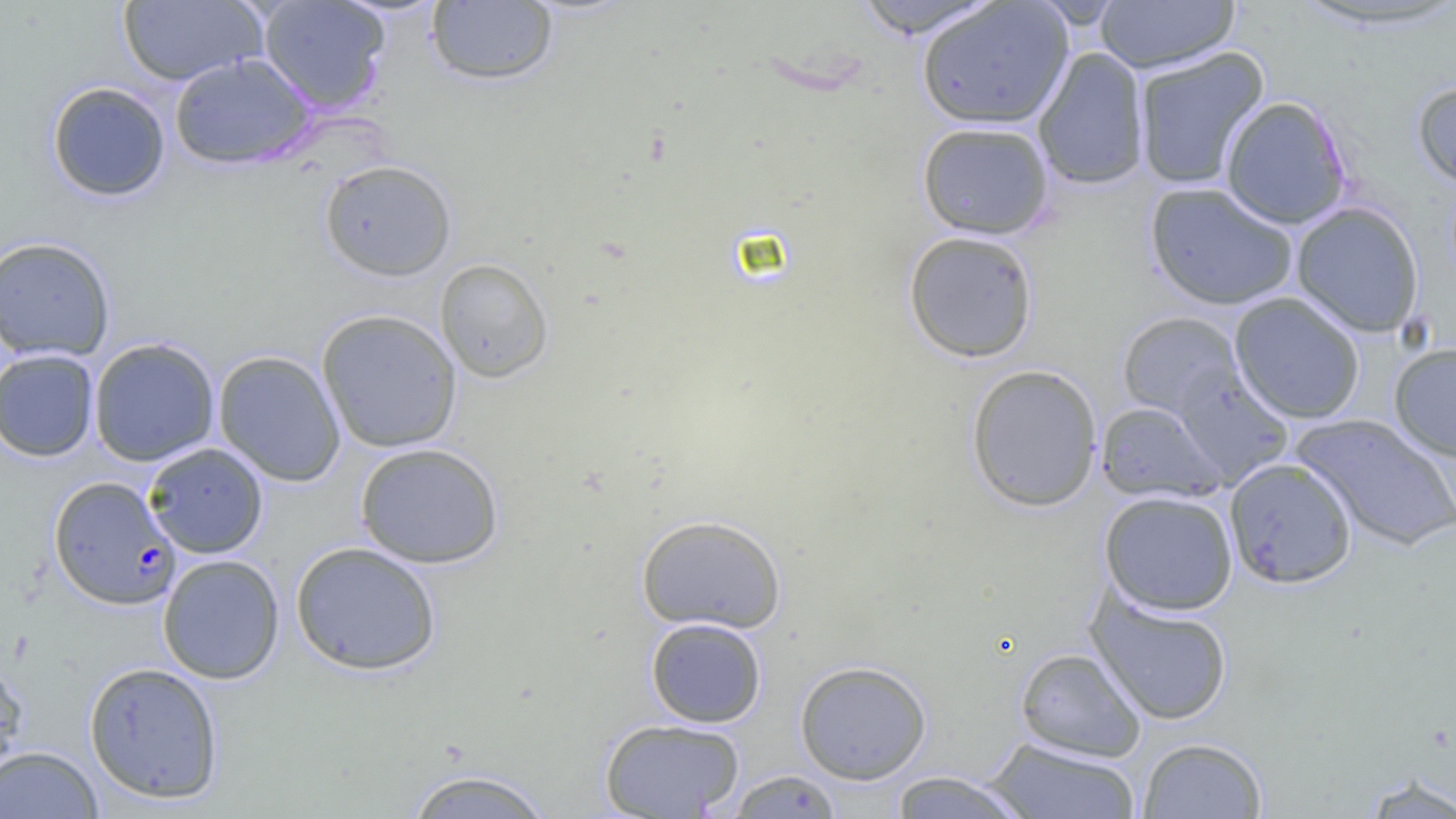

slide-level diagnosis = Plasmodium falciparum
modality = light microscopy
magnification = 1000x
Plasmodium falciparum-infected red blood cell locations = approximate bounding boxes as (x1, y1, x2, y2) in pixels: (49, 476, 180, 610)
uninfected red blood cell locations = approximate bounding boxes as (x1, y1, x2, y2) in pixels: (258, 0, 391, 113), (850, 0, 1004, 38), (1286, 0, 1456, 33), (118, 1, 266, 86), (426, 1, 558, 87), (917, 1, 1074, 130), (1095, 1, 1239, 73), (1132, 46, 1270, 191), (1032, 47, 1151, 189), (170, 54, 316, 170), (1411, 79, 1456, 191), (46, 81, 171, 203), (1220, 96, 1352, 229), (916, 121, 1055, 240), (318, 159, 457, 281), (1144, 182, 1299, 311), (1291, 202, 1425, 338), (903, 230, 1039, 363), (1, 235, 116, 362), (435, 257, 553, 383), (1229, 292, 1366, 424), (316, 309, 463, 453), (1117, 311, 1243, 418), (88, 337, 221, 467), (1389, 342, 1456, 462), (0, 349, 100, 462), (213, 350, 346, 487), (965, 364, 1103, 512), (1171, 365, 1294, 487), (1095, 401, 1226, 504), (1290, 413, 1456, 551), (143, 442, 269, 559), (354, 442, 504, 569), (1224, 457, 1357, 588), (1099, 490, 1238, 615), (635, 514, 788, 634), (290, 541, 442, 675), (157, 554, 285, 684), (1086, 589, 1234, 726), (645, 617, 767, 728), (1015, 647, 1146, 762), (0, 658, 28, 780), (794, 660, 932, 784), (83, 661, 225, 804), (598, 717, 746, 819), (1137, 737, 1268, 818), (983, 738, 1142, 818), (0, 744, 103, 819), (400, 767, 558, 819), (722, 770, 845, 817), (885, 770, 1035, 818), (1358, 774, 1456, 818)
preparation = thin blood smear
image size = 1456×819 pixels
field of view = single